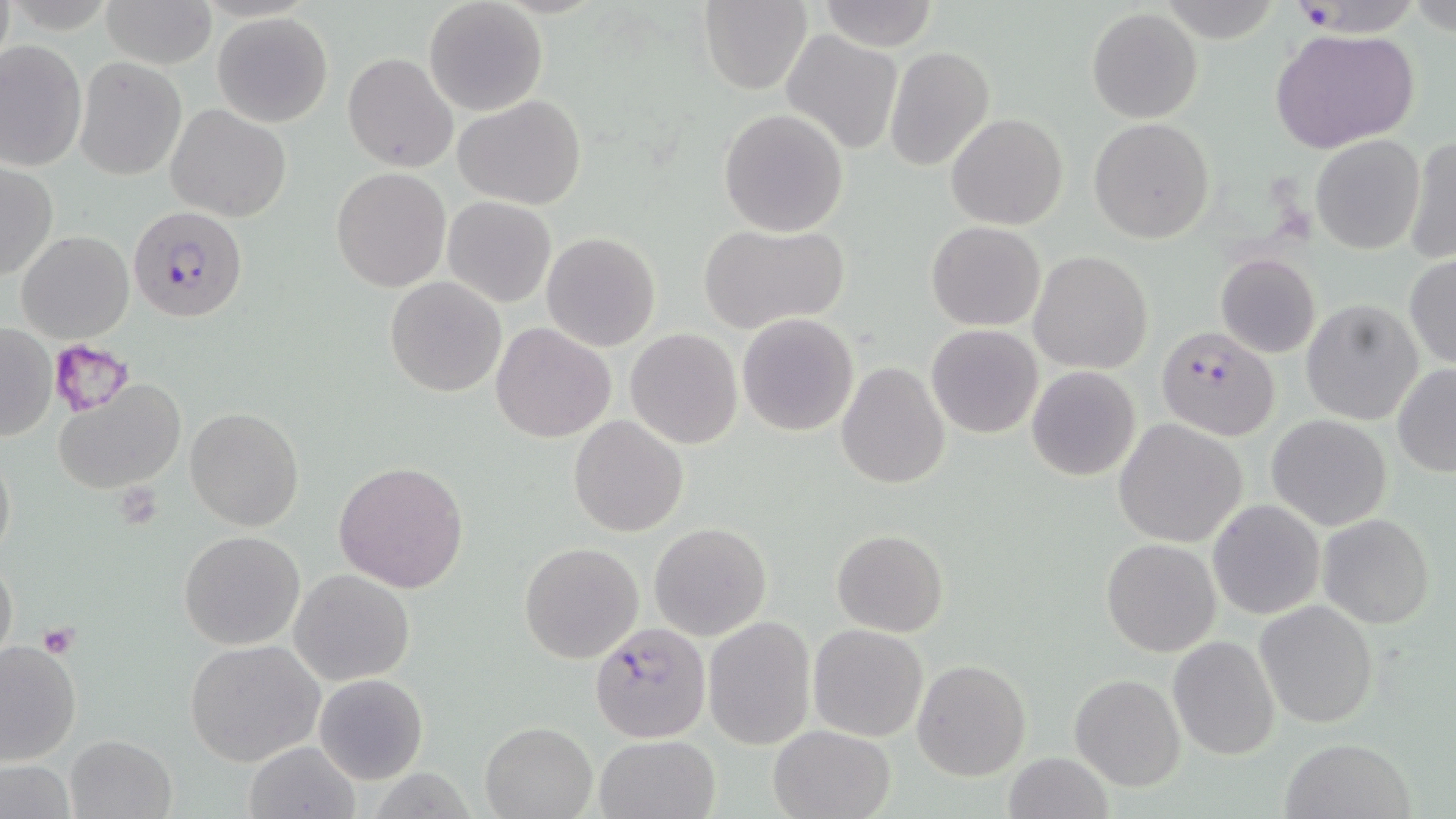
Summary:
  - Coordinate format: approximate bounding boxes as (x1, y1, x2, y2) in pixels
  - Platelet locations: (49, 339, 133, 415), (113, 485, 163, 529), (37, 625, 79, 658)
  - Uninfected red blood cell locations: (423, 0, 547, 116), (700, 0, 814, 94), (1281, 0, 1424, 37), (103, 1, 216, 68), (817, 1, 939, 51), (1087, 8, 1203, 123), (212, 12, 332, 127), (1270, 27, 1422, 156), (780, 30, 904, 155), (0, 37, 87, 174), (885, 46, 994, 172), (342, 52, 459, 173), (75, 57, 186, 180), (452, 95, 588, 207), (166, 104, 290, 221), (718, 109, 849, 237), (946, 113, 1068, 230), (1089, 118, 1214, 243), (1310, 134, 1425, 255), (1405, 136, 1455, 266), (0, 162, 57, 281), (332, 167, 452, 293), (443, 196, 556, 308), (695, 221, 849, 336), (925, 222, 1046, 331), (16, 229, 133, 343), (541, 233, 662, 351), (1028, 251, 1152, 374), (1216, 253, 1320, 358), (1404, 255, 1456, 368), (384, 276, 507, 397), (1301, 299, 1423, 425), (737, 313, 858, 436), (490, 322, 615, 442), (1, 324, 56, 442), (926, 324, 1044, 439), (626, 328, 742, 448), (835, 362, 950, 490), (1392, 365, 1456, 476), (1026, 366, 1141, 481), (53, 379, 187, 495), (185, 407, 305, 530), (1268, 414, 1390, 531), (569, 415, 688, 536), (1115, 418, 1247, 547), (1, 439, 15, 568), (334, 460, 469, 594), (1208, 499, 1326, 621), (1319, 513, 1435, 628), (649, 523, 773, 641), (831, 529, 948, 638), (177, 530, 306, 650), (1101, 538, 1220, 656), (518, 542, 643, 664), (0, 553, 18, 670), (290, 568, 415, 685), (1254, 599, 1378, 729), (703, 615, 815, 749), (808, 623, 929, 742), (1167, 635, 1281, 759), (0, 638, 83, 767), (184, 639, 326, 767), (913, 659, 1031, 781), (315, 673, 428, 784), (1069, 675, 1185, 792), (480, 720, 598, 818), (767, 724, 895, 818), (64, 733, 176, 818), (594, 733, 722, 819), (1279, 736, 1416, 819), (244, 740, 361, 819), (1004, 751, 1113, 819), (0, 758, 78, 818)
  - Plasmodium falciparum-infected red blood cell locations: (128, 204, 250, 323), (1157, 327, 1280, 440), (587, 621, 708, 742)
  - Slide-level diagnosis: Plasmodium falciparum
  - Preparation: thin blood film
  - Modality: optical microscopy
  - Magnification: 1000x
  - Image size: 1456×819 pixels
  - Stain: May-Grünwald-Giemsa
  - Field of view: one of a larger specimen